State which parasite is depicted.
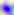
Toxoplasma gondii.

{
  "magnification": "400x",
  "modality": "photomicrograph"
}